Evaluate for Plasmodium parasites.
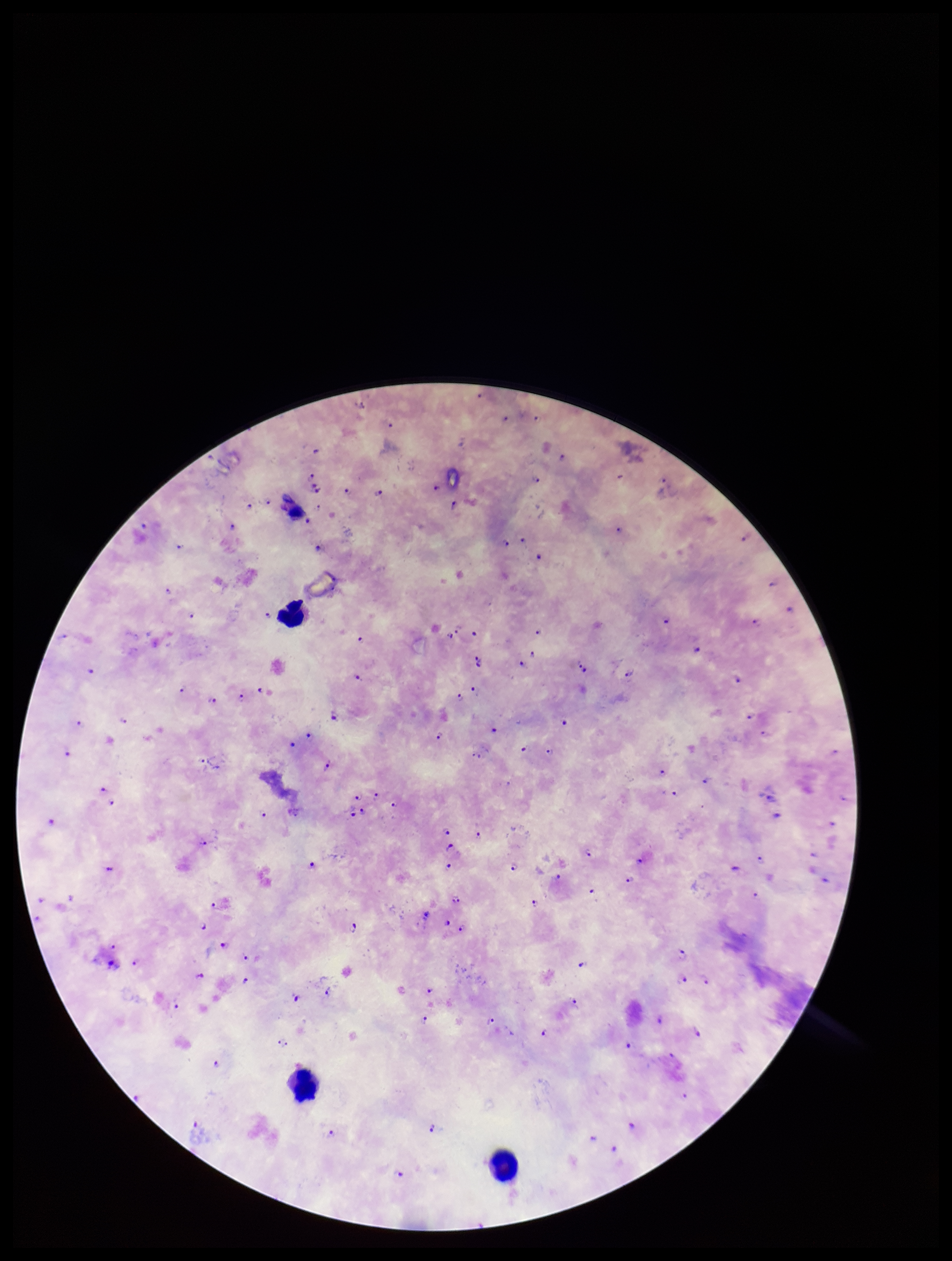

Detected.

Photographed through the microscope eyepiece with a smartphone camera. Species reported for this patient: Plasmodium falciparum. Patient malaria status: infected. One field from this slide. Giemsa stain. Leukocyte count: 4. Image is 952×1261 pixels. Parasite count: 109. Preparation: thick smear.